Outline each uninfected red blood cell.
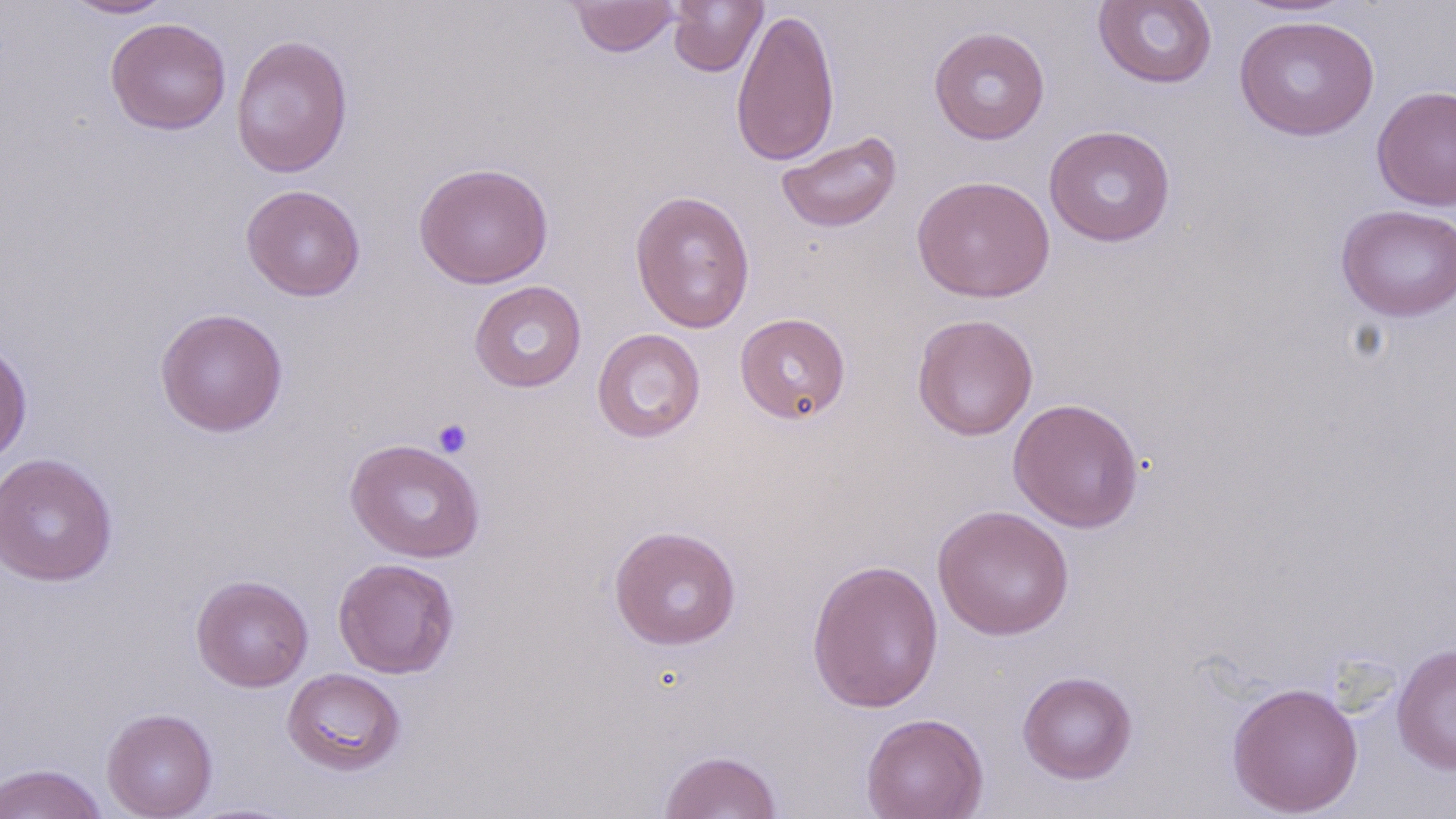
Approximate bounding boxes as named x1/y1/x2/y2 corners in pixels.
Uninfected red blood cells: (x1=62, y1=0, x2=174, y2=19), (x1=1234, y1=0, x2=1355, y2=17), (x1=568, y1=1, x2=680, y2=57), (x1=667, y1=1, x2=768, y2=77), (x1=1092, y1=1, x2=1218, y2=89), (x1=730, y1=7, x2=841, y2=167), (x1=1234, y1=14, x2=1380, y2=141), (x1=105, y1=17, x2=232, y2=135), (x1=929, y1=25, x2=1050, y2=144), (x1=230, y1=33, x2=353, y2=178), (x1=1371, y1=85, x2=1456, y2=211), (x1=1044, y1=124, x2=1176, y2=247), (x1=776, y1=132, x2=902, y2=233), (x1=413, y1=161, x2=554, y2=289), (x1=911, y1=175, x2=1055, y2=303), (x1=241, y1=184, x2=365, y2=301), (x1=629, y1=189, x2=756, y2=334), (x1=1335, y1=204, x2=1456, y2=322), (x1=469, y1=280, x2=587, y2=393), (x1=154, y1=307, x2=289, y2=437), (x1=735, y1=312, x2=851, y2=425), (x1=911, y1=313, x2=1038, y2=441), (x1=592, y1=328, x2=706, y2=443), (x1=0, y1=339, x2=33, y2=465), (x1=1007, y1=397, x2=1145, y2=533), (x1=345, y1=438, x2=486, y2=563), (x1=0, y1=452, x2=118, y2=587), (x1=932, y1=504, x2=1075, y2=640), (x1=608, y1=525, x2=742, y2=651), (x1=332, y1=558, x2=460, y2=679), (x1=806, y1=558, x2=945, y2=713), (x1=190, y1=574, x2=313, y2=692), (x1=1392, y1=642, x2=1456, y2=774), (x1=281, y1=668, x2=406, y2=776), (x1=1017, y1=670, x2=1138, y2=784), (x1=1226, y1=681, x2=1363, y2=817), (x1=101, y1=708, x2=218, y2=818), (x1=861, y1=712, x2=989, y2=819), (x1=658, y1=748, x2=782, y2=819), (x1=0, y1=763, x2=109, y2=819).

Summary:
  - Platelet locations: (x1=432, y1=418, x2=473, y2=458)
  - Slide-level diagnosis: negative for blood parasites
  - Field of view: one of a larger specimen
  - Modality: light microscopy
  - Stain: May-Grünwald-Giemsa
  - Preparation: thin blood smear
  - Image size: 1456×819 pixels
  - Magnification: 1000x